Locate every leukocyte (white blood cell).
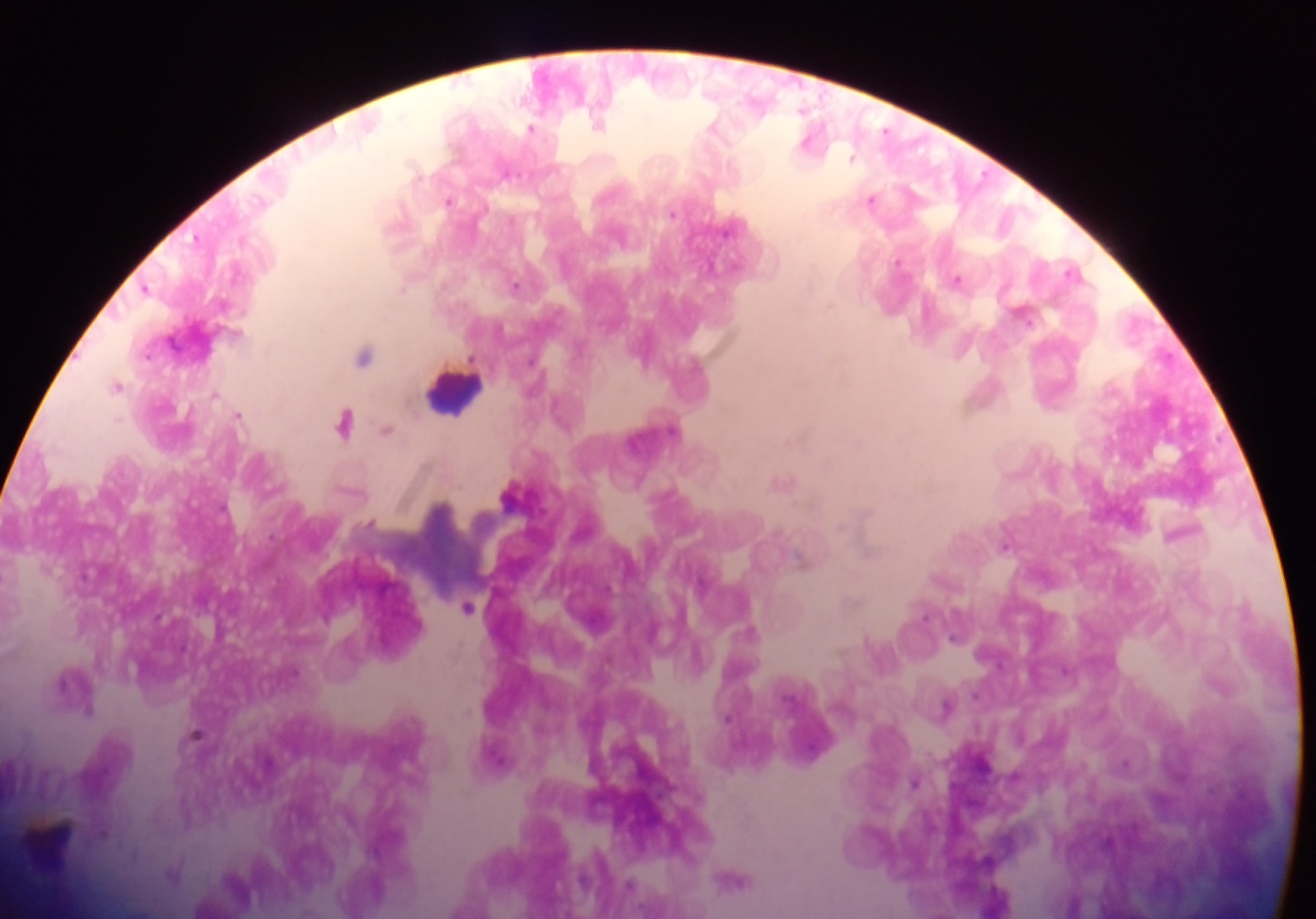

Approximate centers as x y in pixels.
Leukocytes (some below the resolvable threshold): 453 388; 46 852.

Plasmodium parasite locations: 598 123; 531 128; 885 130; 811 137; 852 156; 871 198; 450 200; 672 211; 731 226; 899 261; 1072 270; 957 279; 516 284; 963 346; 365 355; 117 384; 239 414; 345 423; 387 429; 674 429; 370 522; 1006 545; 800 556; 468 606; 751 631; 954 637; 696 656; 63 682; 976 693; 946 705; 90 710; 196 734; 1126 762; 914 781; 1108 840; 986 859; 174 873; 994 903; 1073 907. Single field of view. Photographed through a microscope with a mobile-phone camera. Collected in Ghana. Thick blood smear. Image is 1316×919 pixels.